State which parasite is depicted.
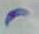

This is Toxoplasma gondii.

Summary:
  - Magnification: 1000x
  - Modality: photomicrograph